Assess this cell for malaria.
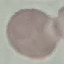

It is uninfected.

stain = Giemsa
preparation = thin blood smear
capture = smartphone camera at the microscope eyepiece
image type = automatically extracted cell patch, resized to 64 × 64 pixels